State the blood parasite species.
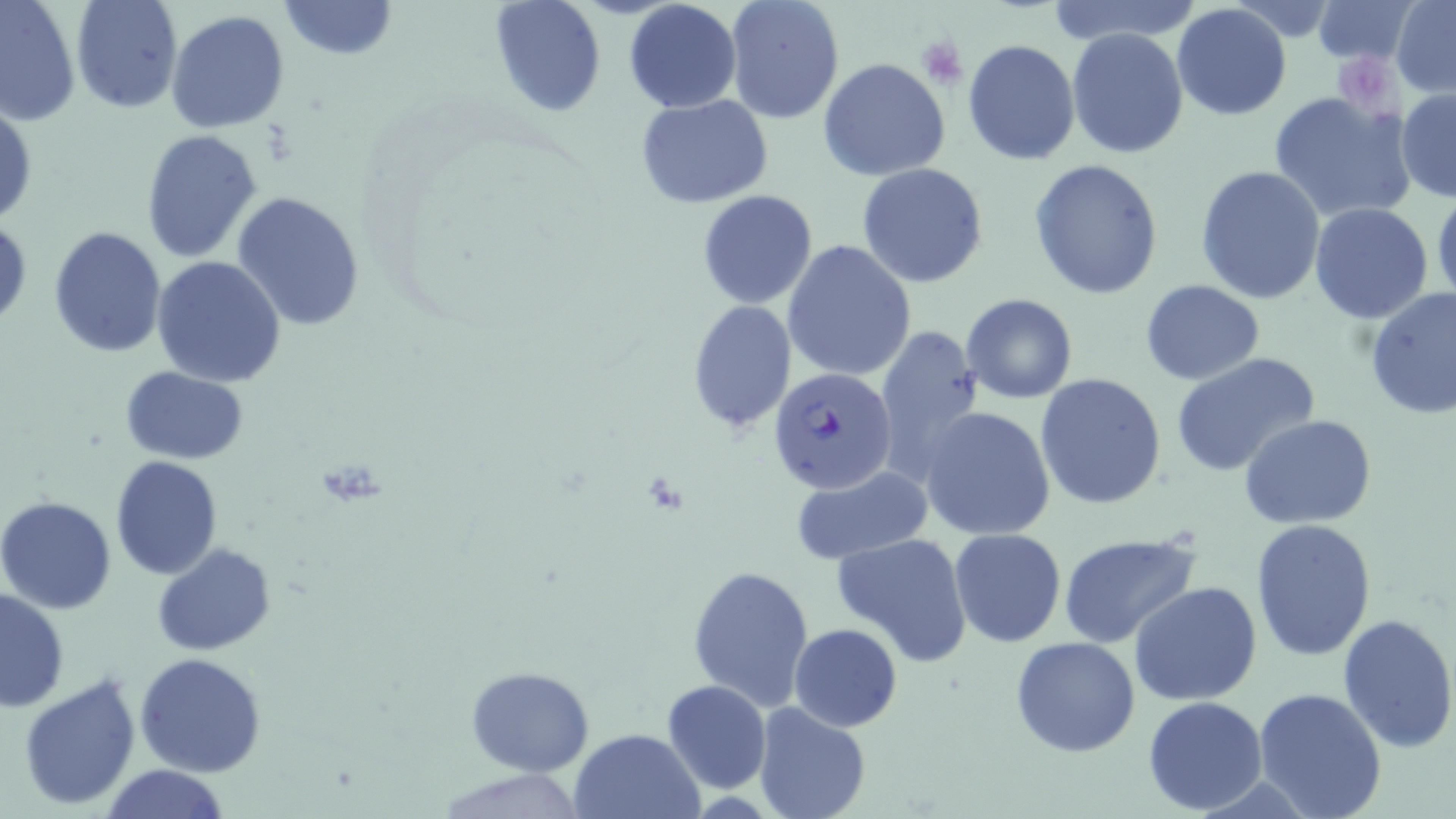
Plasmodium falciparum.

Summary:
  - Coordinate format: approximate bounding boxes as named x1/y1/x2/y2 corners in pixels
  - Plasmodium falciparum-infected red blood cell locations: (x1=769, y1=368, x2=896, y2=495)
  - Platelet locations: (x1=917, y1=34, x2=968, y2=88), (x1=1335, y1=56, x2=1400, y2=112)
  - Uninfected red blood cell locations: (x1=0, y1=0, x2=82, y2=126), (x1=70, y1=0, x2=182, y2=113), (x1=278, y1=0, x2=397, y2=61), (x1=487, y1=0, x2=607, y2=117), (x1=624, y1=0, x2=742, y2=113), (x1=723, y1=0, x2=845, y2=125), (x1=1044, y1=0, x2=1204, y2=48), (x1=1308, y1=0, x2=1421, y2=66), (x1=1391, y1=1, x2=1456, y2=95), (x1=1171, y1=3, x2=1292, y2=120), (x1=166, y1=10, x2=291, y2=132), (x1=1066, y1=27, x2=1189, y2=159), (x1=962, y1=38, x2=1081, y2=165), (x1=818, y1=58, x2=951, y2=182), (x1=1396, y1=88, x2=1456, y2=201), (x1=1268, y1=90, x2=1416, y2=223), (x1=634, y1=94, x2=774, y2=207), (x1=0, y1=101, x2=36, y2=229), (x1=140, y1=128, x2=264, y2=261), (x1=1028, y1=159, x2=1164, y2=301), (x1=857, y1=163, x2=988, y2=287), (x1=1196, y1=164, x2=1326, y2=305), (x1=231, y1=190, x2=368, y2=330), (x1=697, y1=191, x2=819, y2=310), (x1=1431, y1=191, x2=1456, y2=307), (x1=1309, y1=203, x2=1434, y2=322), (x1=0, y1=218, x2=30, y2=331), (x1=47, y1=225, x2=166, y2=360), (x1=782, y1=239, x2=916, y2=381), (x1=151, y1=256, x2=287, y2=386), (x1=1140, y1=280, x2=1266, y2=384), (x1=1364, y1=286, x2=1455, y2=419), (x1=961, y1=294, x2=1077, y2=404), (x1=686, y1=300, x2=796, y2=434), (x1=873, y1=323, x2=986, y2=485), (x1=1170, y1=352, x2=1321, y2=476), (x1=120, y1=366, x2=249, y2=464), (x1=1036, y1=372, x2=1168, y2=509), (x1=919, y1=406, x2=1059, y2=542), (x1=1240, y1=416, x2=1378, y2=529), (x1=109, y1=455, x2=223, y2=580), (x1=790, y1=469, x2=934, y2=565), (x1=0, y1=496, x2=117, y2=614), (x1=1250, y1=518, x2=1376, y2=661), (x1=950, y1=528, x2=1066, y2=647), (x1=832, y1=531, x2=974, y2=666), (x1=1057, y1=531, x2=1202, y2=648), (x1=153, y1=543, x2=275, y2=656), (x1=686, y1=563, x2=815, y2=710), (x1=1129, y1=581, x2=1262, y2=704), (x1=1, y1=589, x2=70, y2=711), (x1=1337, y1=611, x2=1456, y2=753), (x1=788, y1=624, x2=902, y2=731), (x1=1011, y1=635, x2=1142, y2=757), (x1=136, y1=652, x2=267, y2=777), (x1=465, y1=665, x2=593, y2=777), (x1=18, y1=673, x2=143, y2=811), (x1=661, y1=679, x2=772, y2=795), (x1=1253, y1=685, x2=1388, y2=819), (x1=1142, y1=696, x2=1268, y2=814), (x1=753, y1=701, x2=872, y2=819), (x1=569, y1=727, x2=703, y2=818), (x1=97, y1=764, x2=232, y2=819)
  - Magnification: 1000x
  - Stain: May-Grünwald-Giemsa
  - Image size: 1456×819 pixels
  - Field of view: one of a larger specimen
  - Preparation: thin blood film
  - Modality: optical microscopy